Identify the blood parasite species.
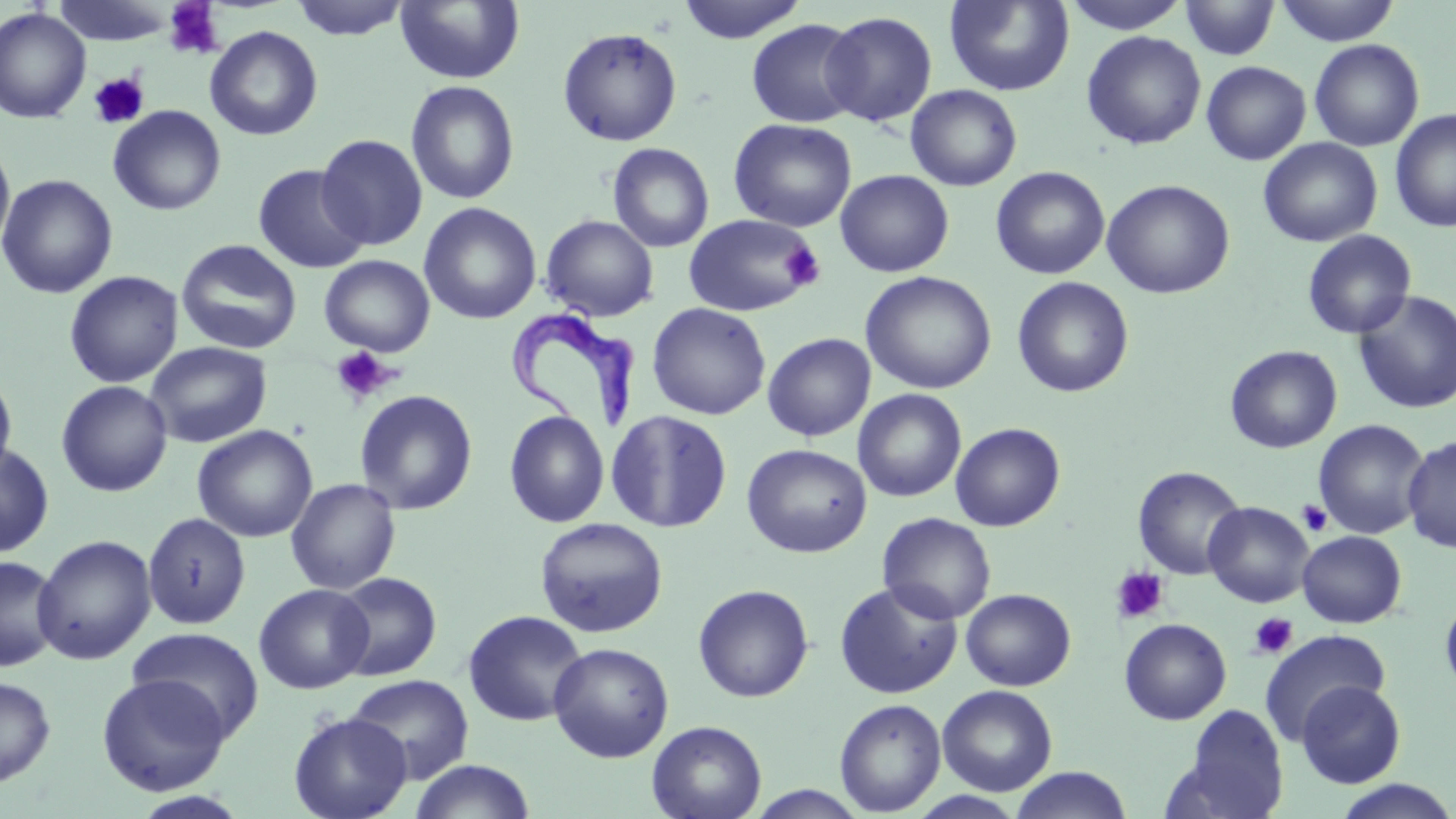

Trypanosoma brucei.

Approximate bounding boxes as (x1, y1, x2, y2) in pixels. Platelet locations: (163, 1, 223, 58), (89, 72, 149, 129), (781, 240, 825, 289), (331, 346, 397, 404), (1297, 500, 1333, 536), (1110, 566, 1169, 624), (1248, 612, 1299, 660). Uninfected red blood cell locations: (53, 0, 177, 46), (289, 0, 411, 40), (675, 0, 809, 43), (944, 0, 1074, 96), (1061, 0, 1190, 34), (1180, 0, 1279, 60), (1274, 0, 1401, 46), (394, 1, 525, 85), (0, 7, 91, 123), (820, 11, 937, 127), (746, 19, 863, 128), (205, 25, 323, 141), (557, 26, 683, 146), (1081, 30, 1206, 150), (1309, 38, 1425, 152), (1201, 61, 1311, 165), (405, 80, 520, 205), (905, 84, 1022, 191), (107, 105, 226, 216), (1389, 108, 1456, 233), (728, 118, 857, 232), (316, 134, 428, 250), (1258, 137, 1382, 247), (0, 140, 16, 259), (607, 142, 714, 252), (252, 164, 370, 274), (990, 166, 1110, 279), (835, 169, 954, 277), (0, 174, 119, 299), (1101, 179, 1235, 299), (419, 202, 541, 324), (683, 213, 821, 318), (540, 215, 659, 321), (1302, 230, 1416, 339), (176, 238, 302, 355), (320, 254, 435, 358), (64, 270, 184, 388), (860, 270, 997, 395), (1012, 276, 1134, 397), (1352, 290, 1456, 415), (647, 302, 771, 420), (762, 332, 876, 442), (144, 341, 273, 448), (1225, 345, 1342, 453), (0, 369, 18, 484), (56, 380, 173, 497), (354, 389, 478, 515), (853, 389, 967, 502), (504, 409, 610, 528), (605, 409, 733, 533), (1313, 419, 1430, 540), (950, 422, 1065, 531), (191, 425, 318, 542), (1402, 435, 1456, 554), (0, 442, 55, 558), (742, 443, 872, 558), (1133, 466, 1247, 580), (286, 477, 401, 594), (1203, 501, 1314, 608), (142, 512, 251, 630), (878, 512, 997, 624), (534, 517, 669, 638), (1297, 530, 1406, 628), (32, 534, 157, 665), (0, 554, 63, 672), (331, 572, 442, 680), (834, 580, 964, 698), (254, 583, 374, 694), (692, 584, 814, 702), (960, 588, 1076, 691), (1440, 595, 1456, 699), (463, 610, 588, 726), (1119, 618, 1232, 725), (127, 626, 264, 741), (1260, 628, 1390, 743), (548, 642, 674, 762), (96, 673, 232, 796), (346, 674, 474, 784), (0, 676, 57, 787), (1295, 680, 1406, 788), (937, 685, 1057, 796), (834, 698, 946, 815), (1173, 704, 1289, 818), (288, 711, 412, 819), (646, 720, 767, 819), (408, 759, 537, 819), (1009, 767, 1134, 819), (1330, 779, 1456, 819), (741, 784, 872, 818), (128, 791, 252, 819), (907, 791, 1027, 818). Trypanosoma brucei locations: (509, 308, 634, 436). 1000x magnification. Single field of view. Thin blood film. May-Grünwald-Giemsa stain. Optical microscopy. Image is 1456×819 pixels.